State the blood parasite species.
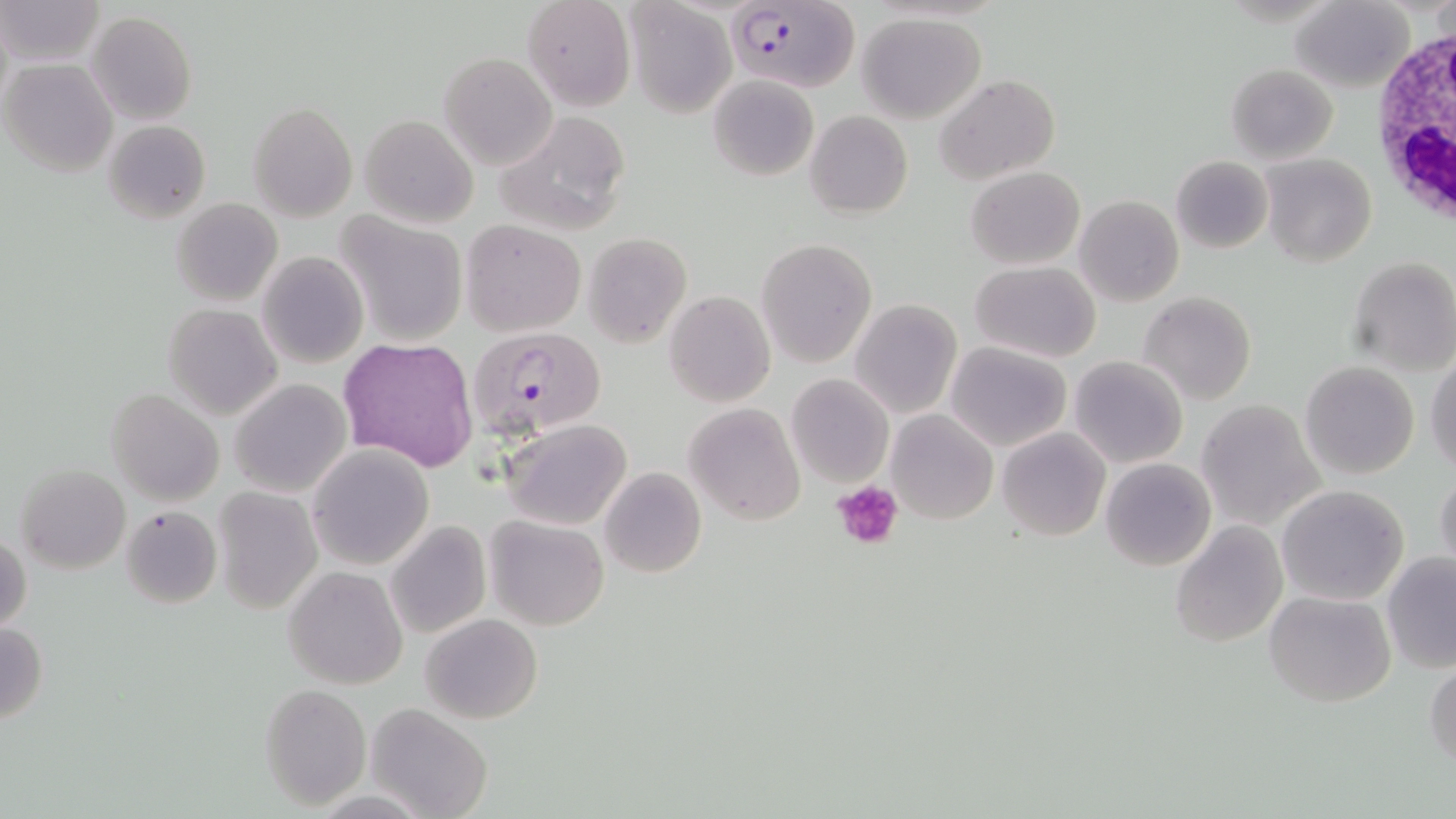

Plasmodium falciparum.

Approximate bounding boxes as [x1, y1, x2, y2] in pixels. White blood cell locations: [1367, 17, 1456, 240]. Plasmodium falciparum-infected red blood cell locations: [725, 0, 858, 94], [466, 326, 608, 443]. Uninfected red blood cell locations: [2, 0, 106, 68], [522, 0, 636, 113], [1291, 0, 1412, 92], [624, 3, 736, 118], [86, 10, 197, 125], [857, 13, 989, 124], [438, 53, 557, 171], [2, 58, 118, 177], [1226, 64, 1338, 163], [934, 73, 1059, 187], [708, 75, 818, 183], [249, 103, 356, 220], [805, 110, 913, 219], [495, 111, 632, 236], [359, 114, 478, 229], [103, 118, 211, 224], [1260, 152, 1376, 269], [1171, 156, 1272, 254], [966, 166, 1085, 268], [1075, 194, 1184, 307], [171, 197, 283, 305], [336, 212, 469, 347], [460, 220, 584, 337], [582, 232, 693, 349], [756, 238, 876, 367], [256, 251, 370, 369], [1348, 254, 1456, 374], [971, 261, 1100, 364], [1139, 291, 1257, 405], [665, 292, 774, 406], [848, 299, 962, 420], [162, 302, 283, 421], [338, 337, 479, 472], [945, 343, 1070, 451], [1426, 350, 1456, 476], [1070, 356, 1187, 469], [1301, 360, 1419, 479], [787, 373, 893, 488], [229, 378, 352, 499], [106, 388, 223, 506], [1196, 401, 1323, 527], [684, 403, 805, 525], [885, 410, 998, 525], [501, 419, 631, 530], [996, 427, 1110, 542], [307, 445, 434, 569], [1101, 457, 1215, 572], [14, 464, 131, 573], [598, 467, 706, 579], [1434, 470, 1456, 580], [1276, 484, 1409, 605], [213, 487, 322, 613], [119, 504, 221, 610], [484, 514, 610, 631], [386, 520, 491, 639], [1170, 522, 1287, 647], [1, 529, 31, 636], [1382, 552, 1456, 672], [283, 566, 406, 689], [1264, 590, 1396, 707], [420, 613, 543, 725], [0, 621, 48, 724], [1424, 656, 1456, 770], [260, 684, 371, 807], [365, 703, 493, 819]. Platelet locations: [832, 482, 902, 550]. 1000x magnification. One field of a larger specimen. Thin blood smear. Optical microscopy. May-Grünwald-Giemsa stain. Image is 1456×819 pixels.